Comment on the morphology of the red blood cells.
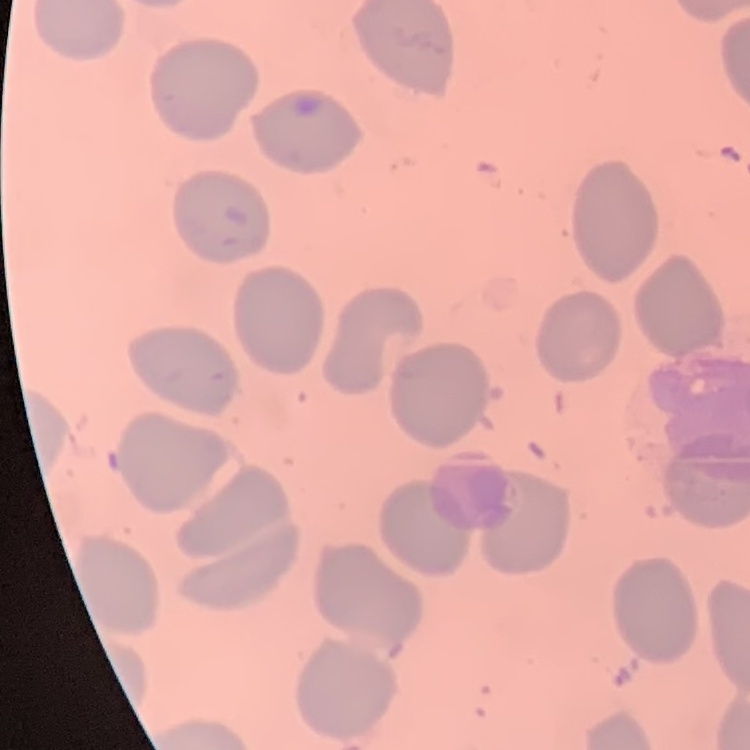
No rouleaux formation.

One tile cut from a larger photomicrograph. Thin blood smear. Field's or Giemsa stain.